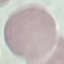 Result: no malaria parasites seen. Automatically extracted cell patch, resized to 64 × 64 pixels. Thin blood smear. Acquired by smartphone through the microscope eyepiece. Giemsa stain.